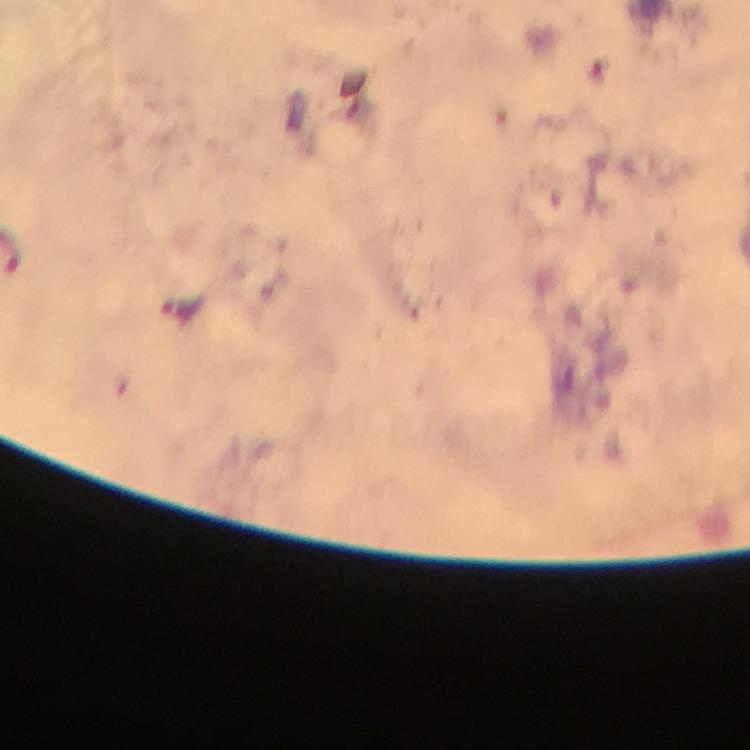
Approximate object centers, in pixels from the top-left corner.
Summary:
  - Plasmodium parasite locations: (x=183, y=307)
  - Immersion oil: used
  - Context: from a malaria diagnostic workup
  - Image size: 750×750 pixels
  - Stain: Giemsa
  - Preparation: thick smear
  - Capture: smartphone camera through the microscope
  - Magnification: 100x
  - Cropped from: one field of view